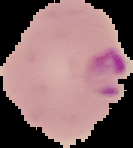
Summary:
  - Image size: 133×148 pixels
  - Result: malaria parasites detected
  - Image type: cell region segmented out of the field of view; surrounding area masked to black
  - Preparation: thin blood film